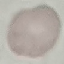

Summary:
  - Malaria status: uninfected
  - Stain: Giemsa
  - Image type: cell patch, automatically extracted from a larger field of view and resized to 64 × 64 pixels
  - Capture: smartphone camera at the microscope eyepiece
  - Preparation: thin smear